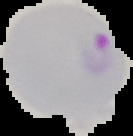

Image is 133×136 pixels. Segmented cell region on a black background. Result: malaria parasites identified. From a thin blood film.